Outline each blood parasite and name the species.
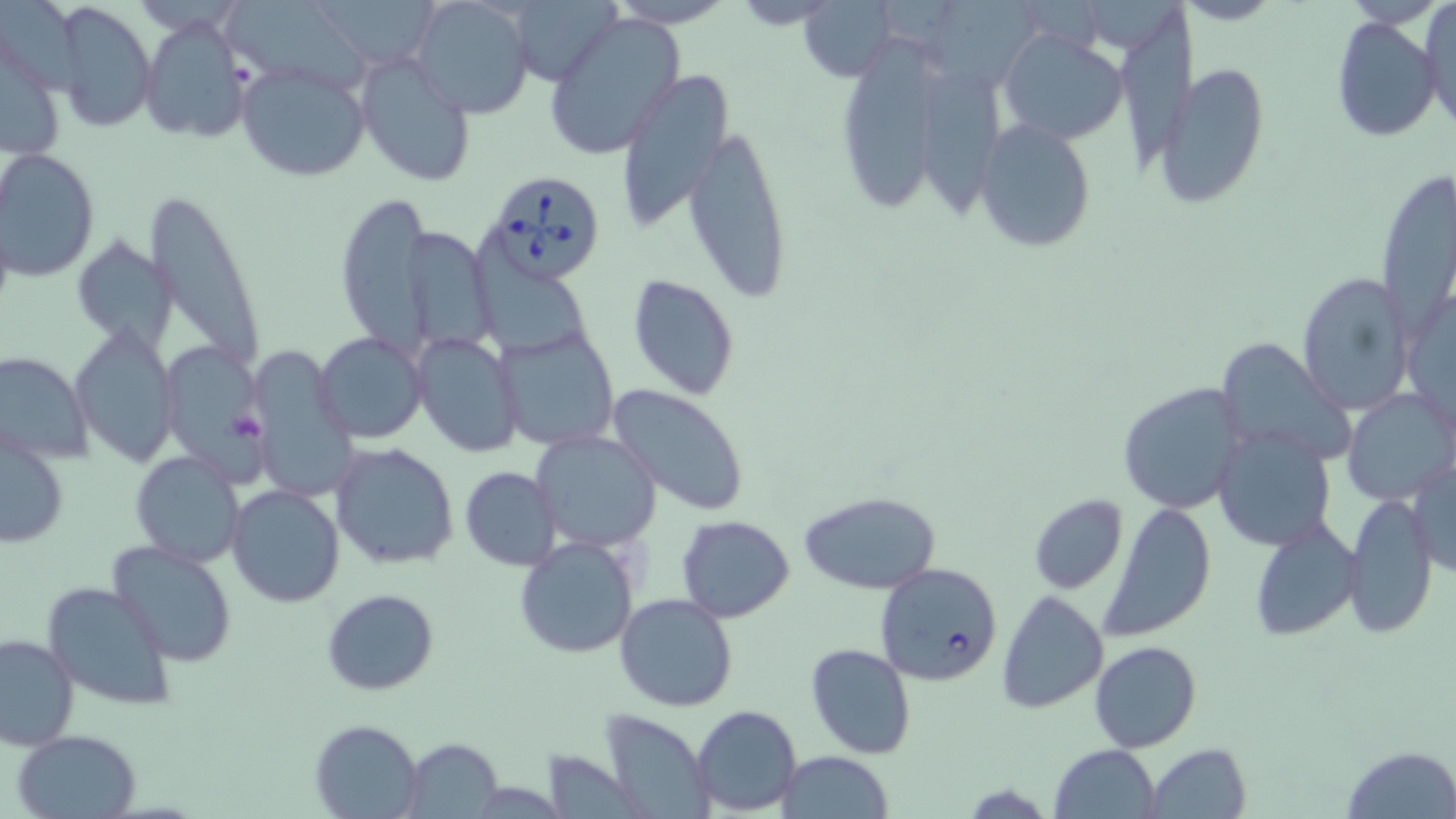
Approximate bounding boxes as (x1,y1)-(x2,y2) corner pairs in pixels.
Babesia divergens-infected red blood cells: (483,168)-(610,284), (873,562)-(1002,685).
No Plasmodium falciparum, Plasmodium ovale, Plasmodium malariae, Plasmodium vivax, or Trypanosoma brucei observed.

Uninfected red blood cell locations: (505,0)-(623,86), (796,0)-(899,82), (921,0)-(1050,92), (218,1)-(375,97), (413,2)-(532,117), (51,3)-(160,129), (1421,3)-(1456,130), (543,13)-(686,160), (1116,13)-(1204,162), (140,15)-(249,143), (1330,17)-(1440,144), (996,28)-(1132,146), (842,36)-(937,214), (356,54)-(479,187), (235,60)-(371,182), (1153,61)-(1271,205), (617,67)-(736,231), (910,70)-(1017,223), (973,117)-(1097,252), (684,125)-(794,303), (3,150)-(100,280), (1374,169)-(1454,332), (144,190)-(266,367), (335,193)-(430,351), (404,226)-(499,352), (469,232)-(592,358), (74,236)-(175,348), (1296,272)-(1415,416), (628,273)-(740,401), (70,326)-(178,468), (495,327)-(621,452), (315,332)-(427,442), (412,333)-(524,458), (159,340)-(269,479), (1222,341)-(1354,466), (249,347)-(356,499), (0,353)-(93,462), (1118,381)-(1250,514), (608,383)-(750,515), (1343,387)-(1455,506), (1212,425)-(1335,552), (530,430)-(662,552), (1,431)-(68,551), (330,442)-(459,570), (128,451)-(246,567), (1407,455)-(1455,580), (459,466)-(560,569), (127,467)-(338,588), (225,483)-(345,608), (798,490)-(942,596), (1027,494)-(1129,595), (1342,494)-(1438,639), (1100,502)-(1215,640), (677,516)-(795,623), (1248,517)-(1362,641), (514,536)-(639,659), (107,539)-(238,667), (40,581)-(177,712), (321,588)-(440,695), (996,589)-(1108,714), (615,593)-(739,712), (0,633)-(77,751), (1088,641)-(1202,752), (806,643)-(916,759), (691,705)-(802,815), (599,710)-(715,817), (310,718)-(423,818), (10,729)-(143,819), (402,737)-(503,817), (1143,743)-(1252,819), (1050,744)-(1160,819), (1341,744)-(1456,818), (775,752)-(894,819). Slide-level diagnosis: Babesia divergens. One field of a larger specimen. Image is 1456×819 pixels. Captured at 1000x magnification. Light microscopy. May-Grünwald-Giemsa-stained preparation. Thin blood smear.